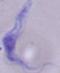 Micrograph. Captured at 1000x magnification. A trypanosome is seen.